Locate every Plasmodium falciparum-infected red blood cell.
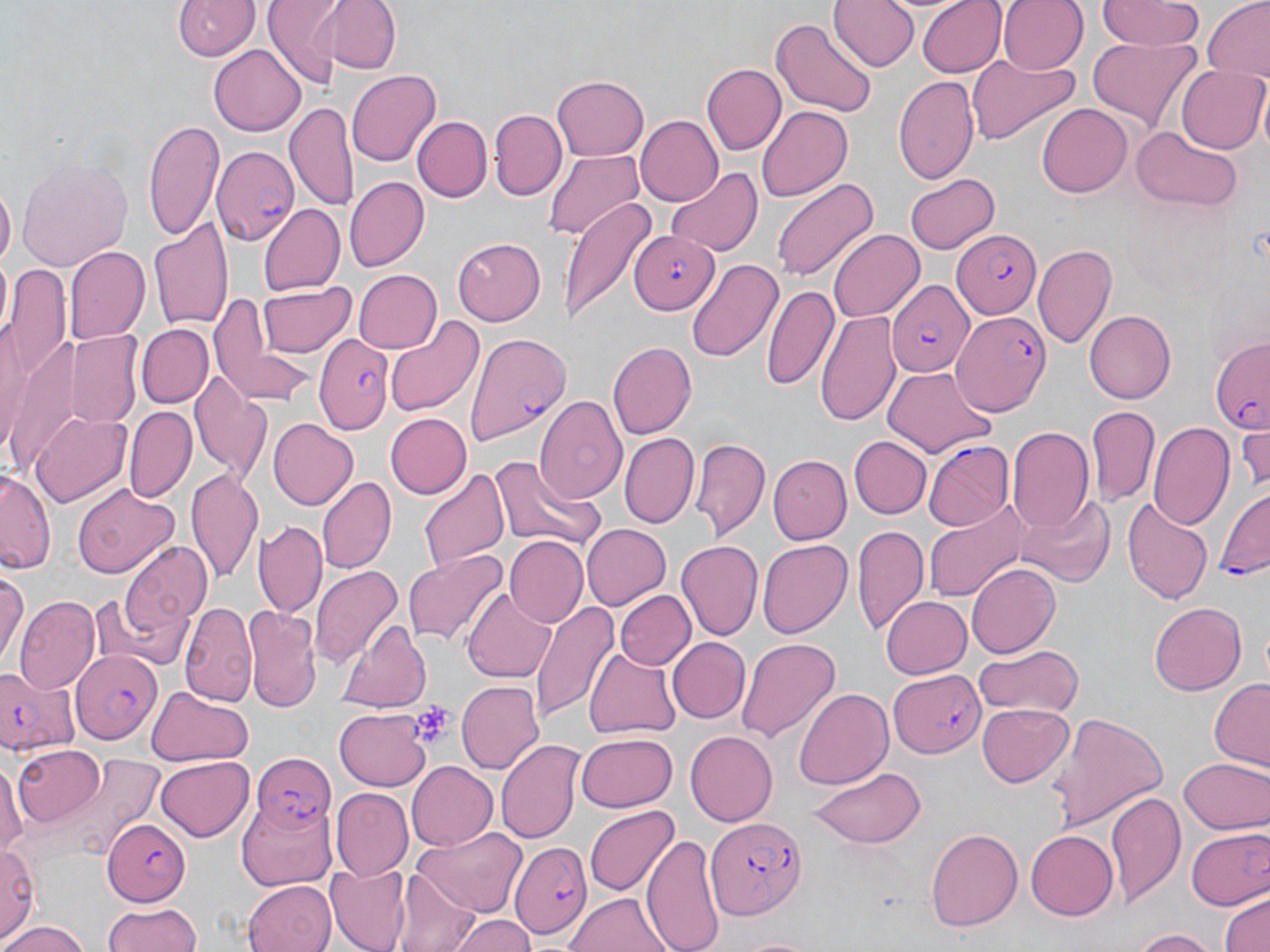
Approximate bounding boxes as (x1, y1, x2, y2) in pixels.
Plasmodium falciparum-infected red blood cells: (213, 146, 299, 246), (950, 227, 1041, 320), (628, 229, 720, 314), (885, 279, 972, 376), (952, 311, 1048, 417), (464, 331, 569, 447), (314, 335, 393, 435), (1208, 335, 1270, 433), (925, 442, 1012, 533), (1215, 487, 1270, 580), (70, 649, 162, 745), (0, 663, 83, 753), (891, 671, 987, 758), (252, 751, 333, 832), (706, 817, 803, 921), (102, 818, 191, 906), (515, 844, 590, 936).

Summary:
  - Platelet locations: (411, 702, 454, 746)
  - Uninfected red blood cell locations: (262, 0, 336, 88), (333, 0, 400, 75), (831, 0, 916, 74), (916, 0, 1005, 76), (997, 0, 1086, 73), (1100, 0, 1203, 50), (174, 1, 256, 61), (1203, 2, 1270, 84), (772, 17, 876, 118), (1088, 37, 1201, 135), (210, 44, 305, 136), (965, 54, 1081, 144), (701, 63, 784, 155), (1177, 66, 1267, 153), (348, 68, 440, 167), (894, 74, 979, 187), (550, 75, 649, 160), (285, 100, 356, 214), (1037, 104, 1132, 198), (756, 105, 850, 202), (489, 107, 568, 200), (411, 115, 492, 201), (636, 115, 724, 205), (142, 118, 226, 239), (1135, 127, 1237, 210), (544, 145, 646, 239), (14, 154, 134, 272), (665, 165, 763, 258), (902, 171, 998, 255), (345, 176, 429, 271), (770, 176, 878, 283), (0, 182, 15, 274), (559, 196, 656, 327), (259, 203, 345, 296), (148, 218, 232, 331), (829, 229, 923, 322), (451, 237, 545, 325), (1034, 244, 1118, 352), (65, 246, 149, 346), (687, 257, 783, 363), (350, 269, 441, 354), (3, 271, 71, 393), (259, 281, 355, 359), (762, 283, 838, 391), (210, 295, 318, 409), (1087, 309, 1176, 403), (816, 311, 898, 426), (383, 315, 484, 421), (137, 323, 212, 407), (63, 330, 146, 428), (608, 342, 695, 439), (883, 367, 996, 457), (190, 369, 272, 482), (535, 395, 625, 504), (125, 405, 195, 501), (1087, 405, 1160, 508), (31, 412, 132, 509), (384, 414, 472, 498), (268, 417, 357, 511), (1149, 421, 1234, 528), (1234, 423, 1270, 495), (1008, 427, 1094, 535), (620, 433, 698, 527), (690, 435, 769, 540), (851, 437, 930, 519), (768, 454, 850, 543), (492, 455, 600, 552), (1, 467, 55, 576), (185, 468, 261, 584), (418, 468, 510, 577), (317, 476, 395, 573), (71, 482, 179, 580), (1014, 493, 1115, 589), (1122, 497, 1213, 605), (924, 498, 1034, 601), (255, 520, 326, 617), (581, 523, 671, 610), (851, 525, 927, 635), (504, 536, 589, 628), (756, 538, 850, 637), (676, 540, 763, 642), (118, 541, 215, 645), (403, 550, 508, 644), (966, 562, 1059, 656), (0, 563, 27, 667), (311, 566, 401, 665), (462, 586, 556, 683), (614, 590, 695, 672), (90, 593, 181, 671), (881, 595, 972, 679), (16, 598, 99, 696), (530, 599, 617, 725), (180, 600, 255, 704), (1149, 601, 1246, 695), (243, 604, 321, 713), (340, 619, 430, 714), (736, 636, 841, 743), (667, 637, 748, 721), (972, 644, 1084, 718), (582, 645, 681, 742), (455, 679, 545, 777), (1209, 679, 1270, 770), (146, 685, 254, 766), (794, 686, 893, 790), (978, 700, 1073, 786), (332, 709, 432, 790), (1048, 709, 1167, 834), (575, 732, 677, 812), (685, 732, 778, 826), (496, 741, 583, 845), (11, 746, 106, 824), (49, 755, 164, 856), (156, 757, 254, 839), (1180, 757, 1269, 833), (0, 760, 28, 859), (406, 761, 498, 851), (809, 765, 926, 849), (332, 789, 413, 880), (1106, 791, 1183, 905), (238, 795, 337, 890), (583, 805, 677, 898), (1185, 825, 1270, 913), (412, 826, 530, 914), (925, 826, 1023, 933), (1025, 828, 1118, 919), (643, 834, 723, 952), (0, 843, 40, 944), (326, 866, 412, 951), (396, 870, 482, 952), (242, 880, 337, 952), (1219, 891, 1270, 952), (566, 893, 671, 951), (100, 905, 203, 951), (451, 913, 535, 952), (1, 919, 92, 951), (1126, 928, 1222, 951), (727, 934, 823, 952)
  - Slide-level diagnosis: Plasmodium falciparum
  - Magnification: 1000x
  - Stain: May-Grünwald-Giemsa
  - Modality: optical microscopy
  - Preparation: thin blood film
  - Image size: 1270×952 pixels
  - Field of view: single